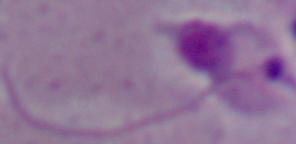
identification = Leishmania
modality = micrograph
magnification = 1000x